Outline each blood parasite and name the species.
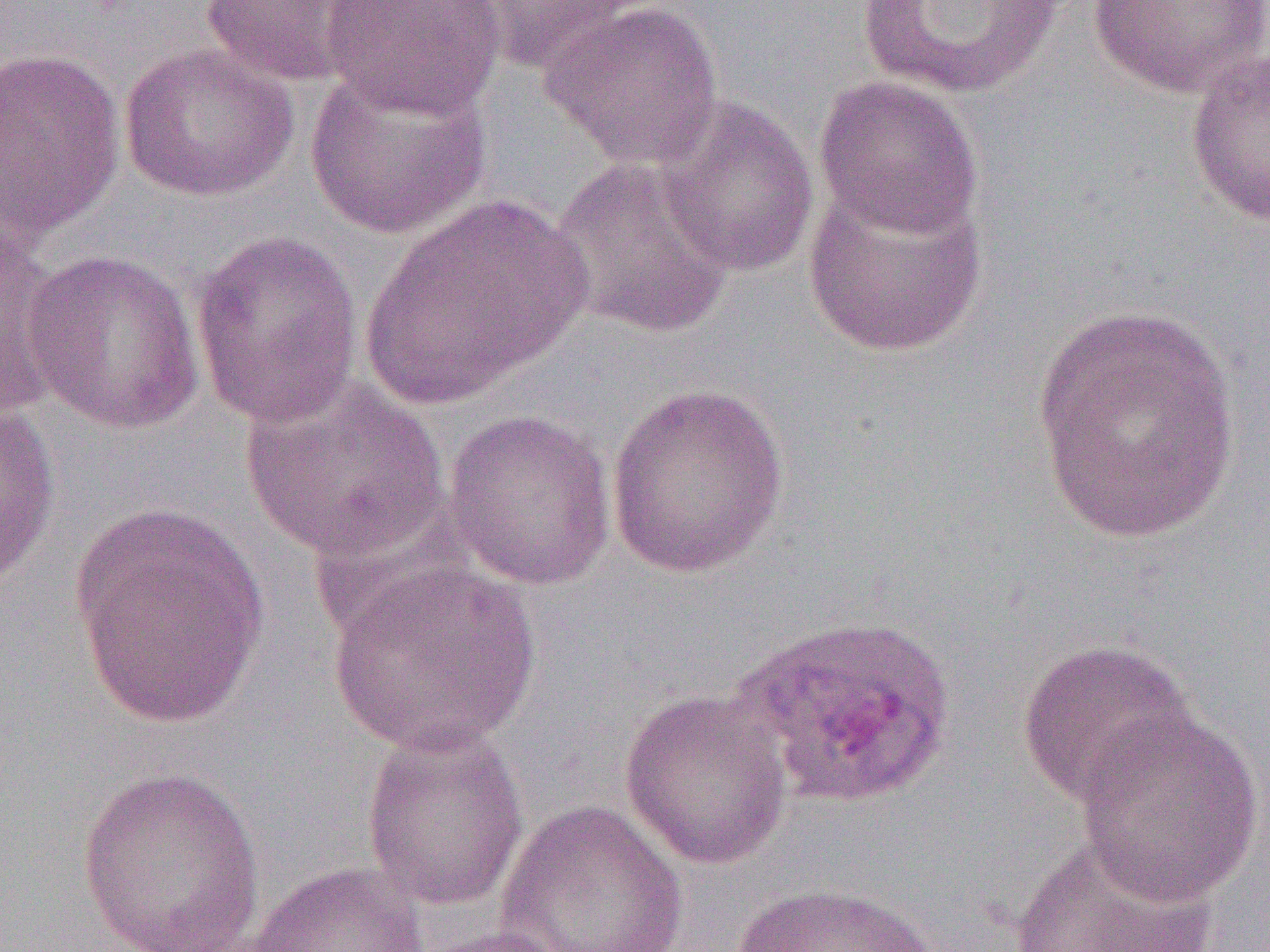

Approximate bounding boxes as [x1, y1, x2, y2] in pixels.
Plasmodium ovale-infected red blood cells: [729, 612, 957, 809].
No Plasmodium falciparum, Plasmodium malariae, Plasmodium vivax, Babesia divergens, or Trypanosoma brucei observed.

slide-level diagnosis = Plasmodium ovale
modality = optical microscopy
preparation = thin blood smear
field of view = one of a larger specimen
image size = 1270×952 pixels
uninfected red blood cell locations = approximate bounding boxes as [x1, y1, x2, y2] in pixels: [198, 0, 379, 86], [321, 0, 507, 119], [541, 0, 723, 170], [849, 0, 1075, 101], [458, 1, 662, 73], [1087, 1, 1270, 99], [120, 42, 299, 202], [0, 46, 126, 242], [1185, 46, 1270, 230], [304, 65, 493, 241], [813, 74, 984, 240], [656, 96, 820, 279], [548, 155, 736, 340], [801, 180, 989, 359], [362, 192, 590, 410], [0, 217, 65, 420], [191, 228, 365, 429], [20, 247, 205, 434], [1029, 301, 1240, 544], [240, 376, 451, 564], [606, 382, 790, 579], [1, 398, 61, 593], [441, 408, 618, 590], [67, 502, 274, 732], [325, 560, 543, 756], [1016, 637, 1199, 811], [619, 688, 793, 870], [1072, 711, 1266, 906], [360, 723, 529, 912], [76, 766, 265, 950], [494, 798, 690, 952], [1008, 835, 1220, 952], [237, 861, 430, 952], [729, 882, 940, 952], [403, 924, 574, 952]
magnification = 1000x